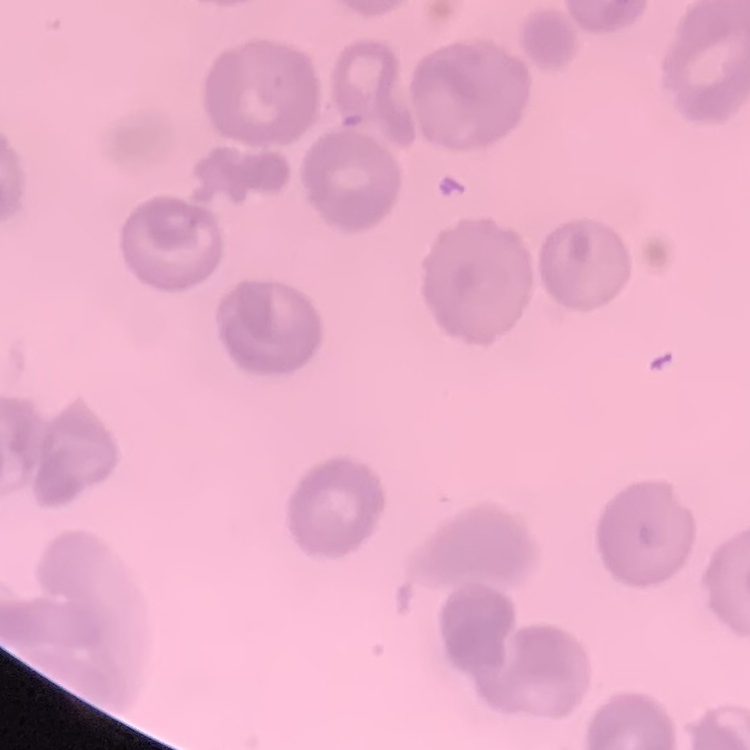
The red blood cells show no rouleaux formation. Thin blood film. One tile cut from a larger photomicrograph. Field's or Giemsa stain.